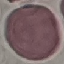

malaria status = uninfected
capture = smartphone through the microscope eyepiece
image type = cell patch, automatically extracted from a larger field of view and resized to 64 × 64 pixels
stain = Giemsa
preparation = thin blood smear